Outline each blood parasite and name the species.
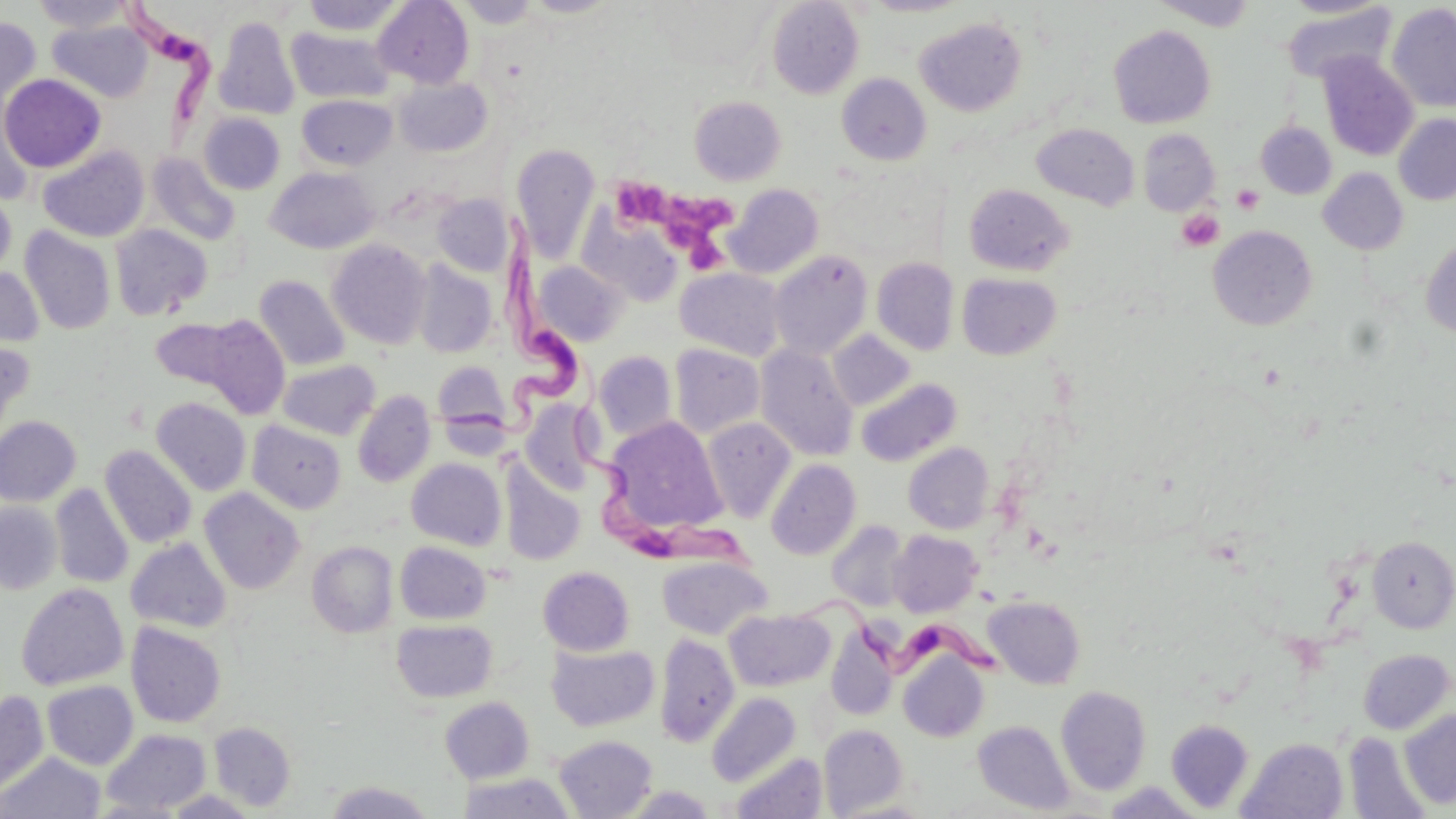

Approximate bounding boxes as (x1, y1, x2, y2) in pixels.
Trypanosoma brucei: (121, 5, 235, 143), (450, 208, 587, 446), (564, 397, 768, 585), (808, 597, 1011, 698).
No Plasmodium falciparum, Plasmodium ovale, Plasmodium malariae, Plasmodium vivax, or Babesia divergens observed.

Uninfected red blood cell locations: (31, 0, 134, 33), (301, 0, 404, 35), (373, 0, 474, 88), (455, 0, 543, 28), (519, 0, 623, 18), (646, 0, 773, 72), (861, 0, 972, 17), (1152, 0, 1258, 30), (1280, 0, 1390, 19), (766, 1, 864, 98), (1386, 3, 1456, 112), (1282, 6, 1397, 82), (214, 16, 300, 120), (0, 17, 40, 119), (915, 18, 1027, 115), (48, 20, 152, 101), (1109, 25, 1216, 129), (286, 27, 393, 103), (1317, 52, 1419, 161), (1, 73, 106, 173), (837, 73, 932, 165), (392, 76, 494, 157), (297, 94, 397, 170), (689, 96, 787, 185), (198, 112, 285, 194), (1394, 114, 1456, 206), (1256, 121, 1336, 199), (1032, 123, 1139, 210), (1137, 128, 1220, 215), (511, 143, 600, 263), (38, 145, 150, 242), (146, 152, 241, 246), (265, 166, 379, 254), (1318, 167, 1409, 254), (964, 183, 1074, 275), (724, 184, 824, 278), (0, 186, 16, 280), (432, 194, 513, 276), (582, 208, 684, 306), (109, 224, 212, 320), (19, 226, 116, 335), (1208, 226, 1317, 330), (1420, 237, 1456, 339), (326, 239, 432, 349), (769, 250, 872, 359), (871, 258, 958, 355), (411, 259, 497, 358), (532, 260, 627, 346), (0, 265, 44, 348), (675, 267, 787, 360), (957, 272, 1062, 359), (254, 275, 350, 371), (203, 315, 291, 419), (150, 317, 244, 392), (828, 330, 915, 411), (0, 334, 35, 447), (670, 343, 765, 437), (755, 345, 859, 461), (593, 350, 678, 441), (277, 359, 380, 440), (432, 361, 512, 432), (855, 378, 962, 467), (353, 390, 436, 487), (151, 397, 251, 496), (520, 400, 597, 495), (0, 416, 81, 506), (603, 417, 728, 537), (701, 417, 796, 522), (247, 421, 347, 513), (903, 442, 994, 533), (100, 445, 196, 548), (407, 458, 507, 550), (766, 459, 861, 560), (499, 460, 586, 566), (50, 484, 133, 588), (199, 487, 305, 594), (0, 501, 63, 594), (826, 519, 910, 612), (888, 530, 983, 617), (1367, 536, 1456, 633), (126, 538, 232, 633), (307, 541, 398, 638), (395, 541, 491, 624), (657, 555, 771, 639), (538, 566, 634, 656), (16, 583, 128, 690), (983, 595, 1086, 689), (725, 609, 833, 691), (391, 619, 498, 703), (126, 622, 226, 728), (827, 628, 897, 721), (654, 633, 738, 747), (547, 643, 659, 731), (1358, 649, 1454, 734), (898, 651, 989, 743), (42, 680, 138, 769), (1056, 685, 1151, 795), (0, 689, 49, 800), (707, 692, 801, 787), (439, 696, 534, 783), (1399, 709, 1456, 810), (1165, 719, 1254, 813), (974, 720, 1075, 814), (209, 722, 295, 811), (818, 723, 908, 816), (101, 728, 211, 815), (1345, 731, 1433, 819), (554, 735, 657, 818), (1237, 738, 1347, 819), (0, 752, 105, 818), (731, 752, 827, 819), (456, 772, 577, 818), (323, 781, 436, 819), (1103, 782, 1206, 818), (620, 786, 718, 818). Platelet locations: (618, 180, 677, 229), (1232, 184, 1264, 214), (670, 198, 731, 235), (1176, 209, 1223, 252), (682, 230, 729, 275). Slide-level diagnosis: Trypanosoma brucei. Optical microscopy. May-Grünwald-Giemsa stain. One field of a larger specimen. Thin blood smear. 1000x magnification. Image is 1456×819 pixels.